Give the extent of all uninfected red blood cells.
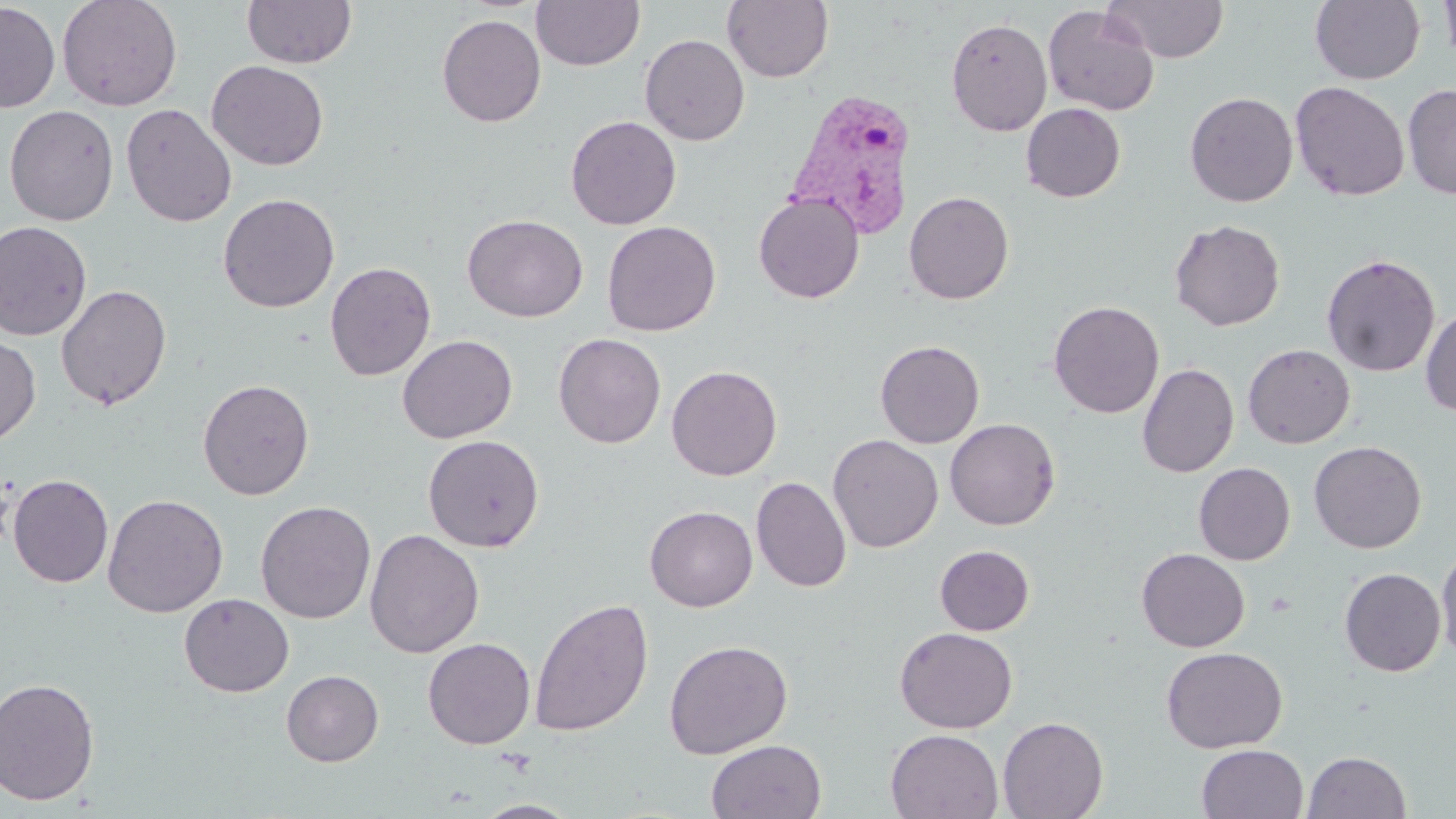
Approximate bounding boxes as (x1,y1)-(x2,y2) corner pairs in pixels.
Uninfected red blood cells: (57,0)-(183,112), (241,0)-(357,69), (530,0)-(645,71), (721,0)-(835,83), (1106,0)-(1230,62), (1310,0)-(1425,85), (1439,0)-(1456,70), (0,2)-(60,113), (1042,4)-(1159,115), (436,14)-(546,127), (946,17)-(1052,136), (640,33)-(750,146), (207,60)-(329,170), (1290,81)-(1410,202), (1402,83)-(1456,199), (1185,92)-(1298,207), (121,103)-(237,228), (1021,103)-(1125,202), (4,104)-(119,226), (565,115)-(681,230), (904,191)-(1014,304), (753,192)-(864,303), (218,193)-(340,313), (463,214)-(588,322), (1169,219)-(1285,331), (601,220)-(721,336), (0,221)-(93,341), (1321,254)-(1440,377), (324,261)-(437,381), (56,284)-(172,410), (1048,300)-(1164,418), (1420,305)-(1456,417), (0,332)-(40,446), (553,333)-(666,448), (397,334)-(518,443), (875,340)-(985,448), (1242,343)-(1355,448), (1137,363)-(1239,478), (666,365)-(782,481), (197,378)-(315,500), (944,418)-(1060,530), (423,434)-(545,553), (827,434)-(943,552), (1308,440)-(1427,553), (1194,462)-(1295,565), (7,474)-(114,588), (752,476)-(851,593), (102,494)-(229,618), (255,500)-(376,624), (645,505)-(758,612), (364,528)-(484,659), (1436,543)-(1456,662), (934,544)-(1034,635), (1136,548)-(1250,652), (1339,567)-(1446,677), (178,593)-(294,697), (529,597)-(654,737), (895,627)-(1017,733), (422,637)-(535,749), (663,638)-(793,759), (1160,646)-(1287,752), (280,669)-(384,767), (0,676)-(101,807), (997,716)-(1108,819), (886,729)-(1004,818), (706,739)-(827,819), (1197,744)-(1308,819), (1302,751)-(1412,818), (471,800)-(582,818).

Plasmodium vivax-infected red blood cell locations: (784,87)-(919,239). Slide-level diagnosis: Plasmodium vivax. Optical microscopy. May-Grünwald-Giemsa stain. Captured at 1000x magnification. Image is 1456×819 pixels. Thin blood film. Single field of view.